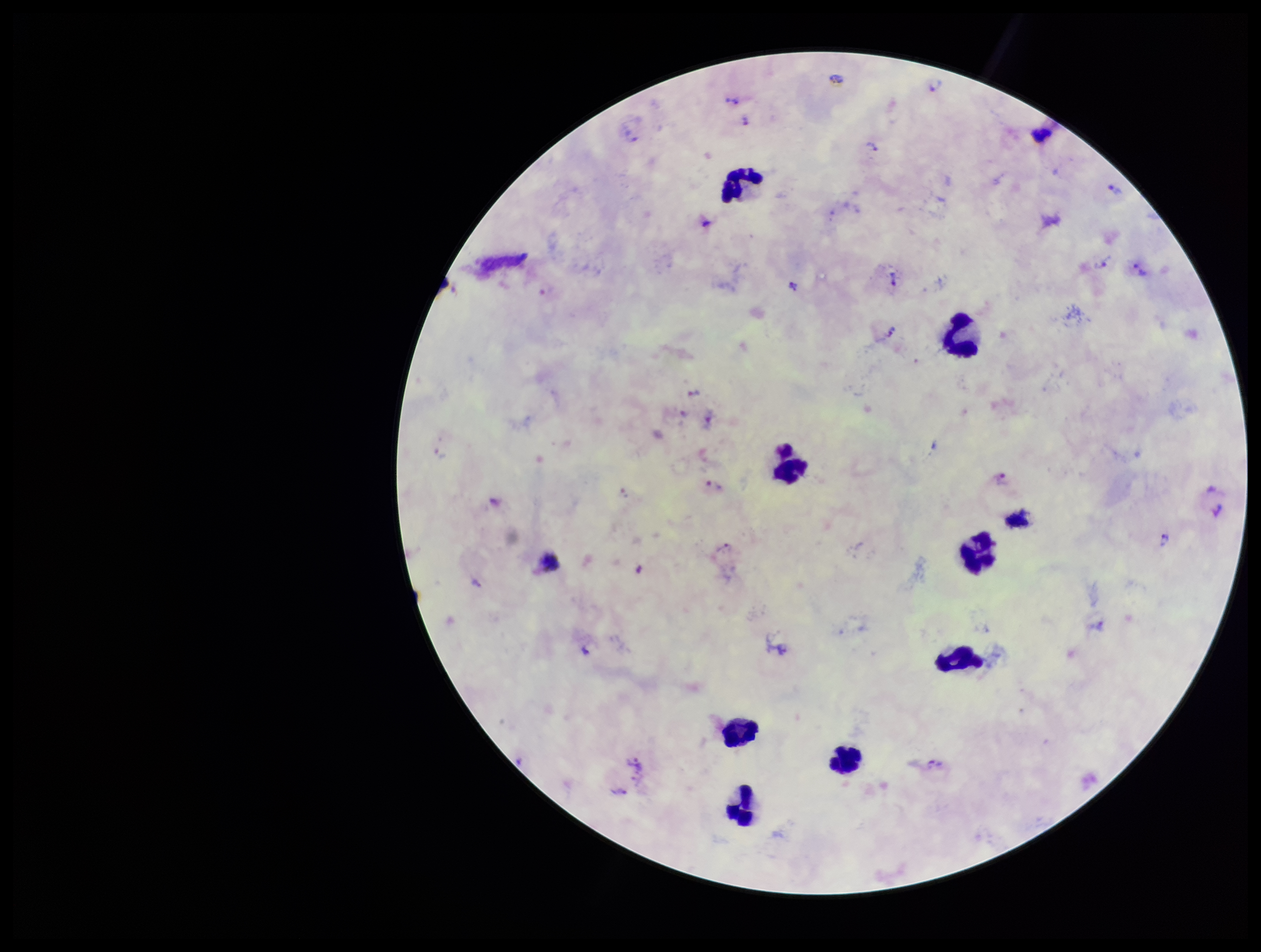

leukocyte_count: 9
image_size: 1261×952 pixels
parasite_count: 21
species_reported_for_this_patient: Plasmodium vivax
capture: smartphone photograph through the microscope eyepiece
plasmodium_parasites: seen
patient_malaria_status: positive
field_of_view: single
stain: Giemsa
preparation: thick smear